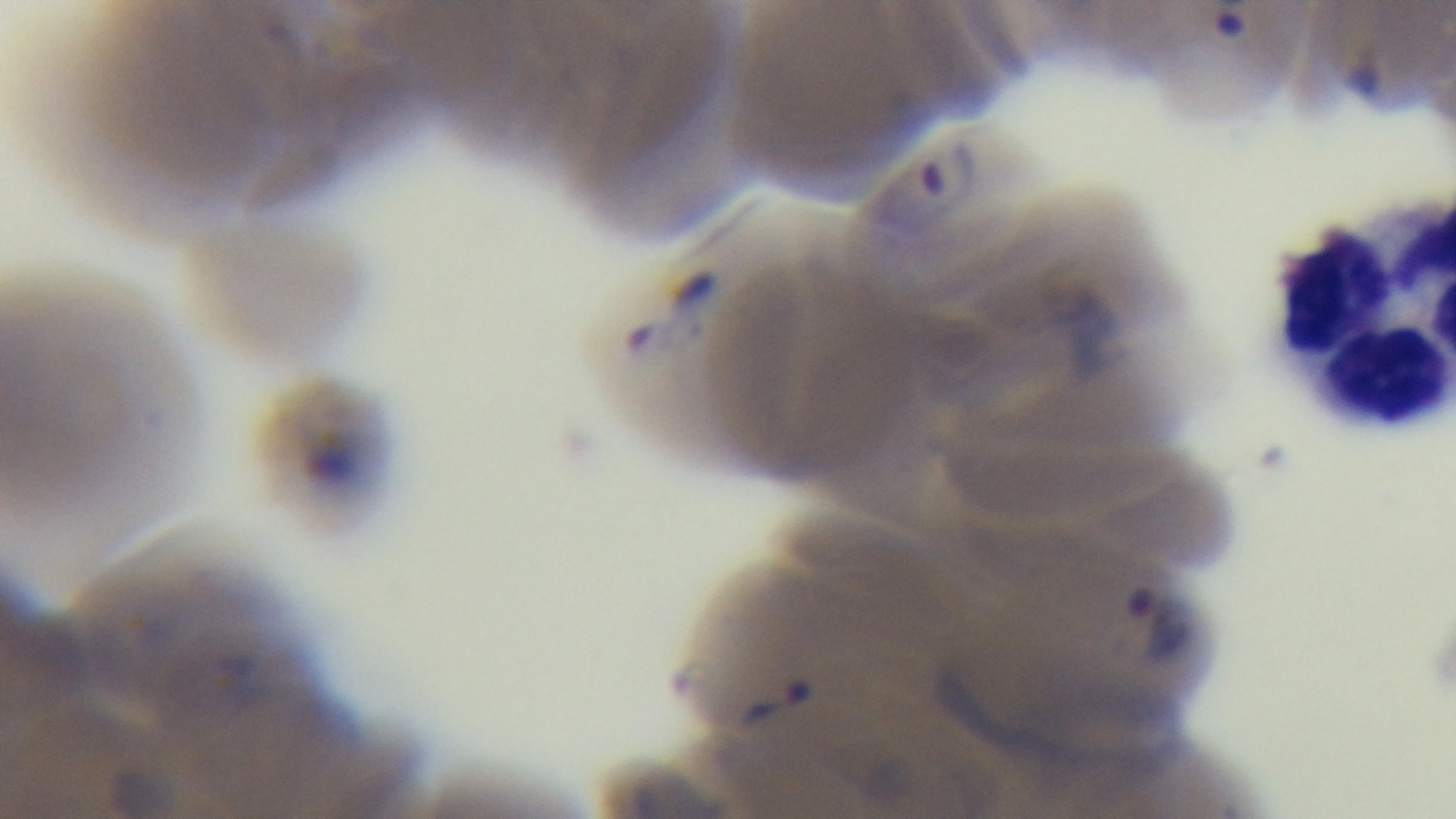 Malaria status: positive. Oil-immersion objective, 100x. Single field of view. Photomicrograph. Mounted 4K digital camera. Preparation: thin smear. Giemsa-stained.